Report the malaria status of this cell.
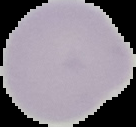

It is uninfected.

image size = 136×127 pixels
image type = cell region segmented out of the field of view; surrounding area masked to black
preparation = thin blood film